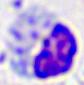
identification: leukocyte
modality: photomicrograph
magnification: 400x